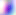
Summary:
  - Magnification: 400x
  - Modality: micrograph
  - Identification: Toxoplasma gondii